Identify the preparation type.
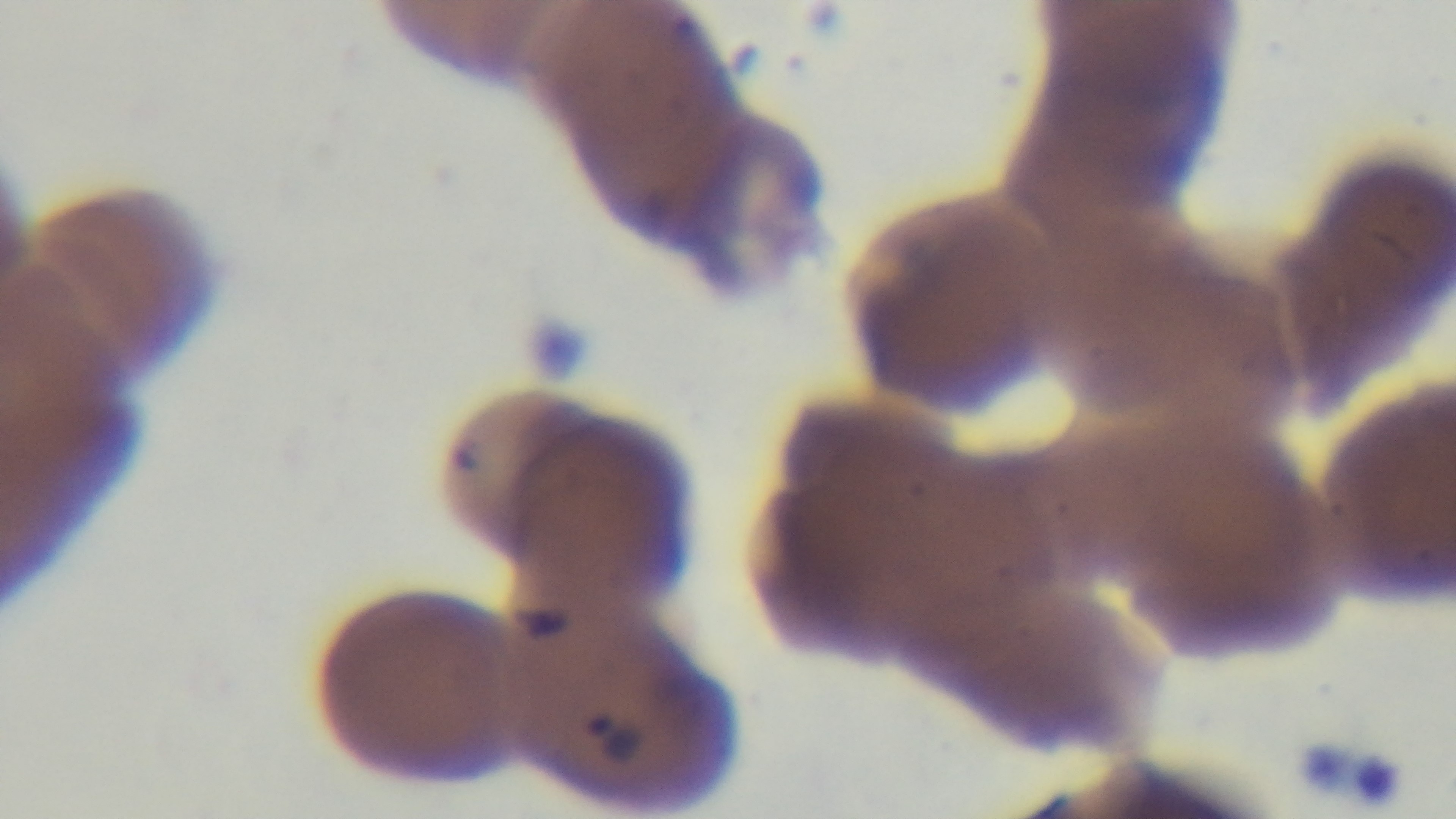

It is a thin blood film.

Mounted 4K digital camera. 100x oil-immersion objective. Single field of view. Photomicrograph. Giemsa stain. Malaria status: infected.